State which parasite is depicted.
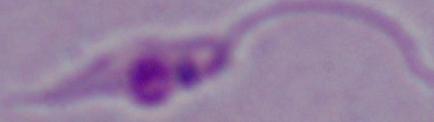
Leishmania.

Photomicrograph. Captured at 1000x magnification.